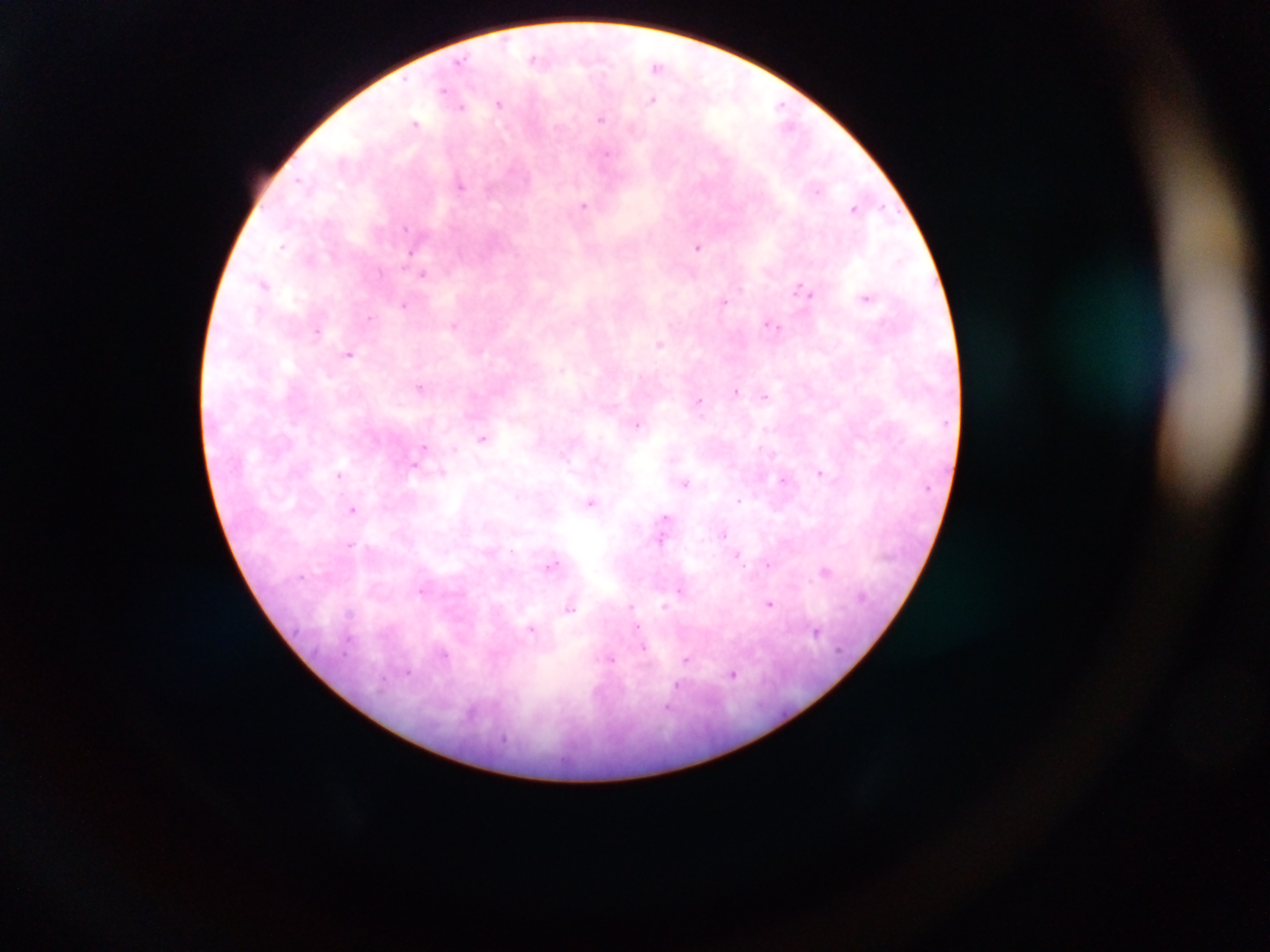

plasmodium_parasite_locations: 'approximate centers as x y in pixels: 534 58; 460 61; 657 66; 443 90; 652 100; 499 103; 780 106; 461 107; 601 118; 415 123; 604 157; 300 181; 460 185; 816 191; 584 206; 854 208; 405 227; 282 245; 698 247; 409 253; 380 272; 422 275; 264 284; 802 290; 867 298; 723 302; 404 305; 370 318; 454 325; 772 326; 316 332; 660 344; 348 354; 562 369; 421 387; 736 391; 765 396; 699 401; 638 425; 482 438; 424 448; 454 449; 414 466; 442 473; 821 473; 339 475; 784 480; 685 483; 517 495; 739 499; 590 503; 352 509; 665 518; 664 526; 723 534; 661 538; 351 544; 738 556; 552 565; 768 565; 826 572; 679 590; 769 605; 664 606; 569 608; 348 613; 636 629; 531 630; 815 631; 348 640; 644 648; 444 654; 610 660; 687 660; 407 671; 733 674; 678 687; 668 707'
preparation: thick blood smear
image_size: 1270×952 pixels
country: Ghana
field_of_view: single
capture: mobile-phone photograph through a microscope